Locate every leukocyte (white blood cell).
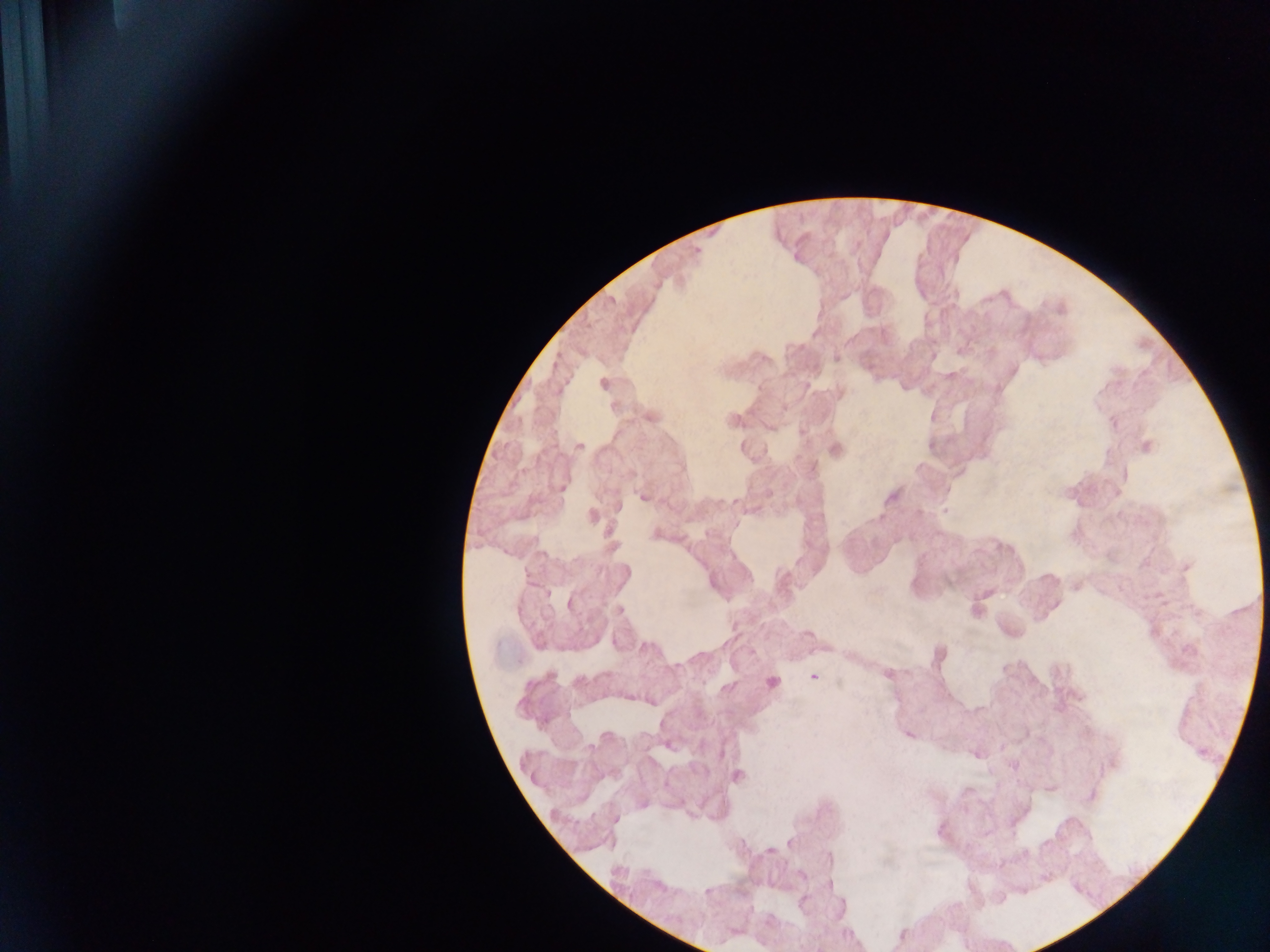
Approximate centers as x y in pixels.
Leukocytes: 603 382; 1147 446; 979 611; 774 683.

country: Ghana
preparation: thick blood film
image_size: 1270×952 pixels
malaria_parasite_locations: 'approximate centers as x y in pixels: 579 446; 642 497; 592 516; 656 534; 985 594; 807 634; 887 675; 813 677; 737 776'
field_of_view: single
capture: mobile-phone photograph through a microscope